Classify this cell by malaria status.
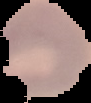

Parasitized.

preparation: thin blood film
image_size: 91×103 pixels
image_type: segmented cell region with the area outside set to black